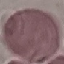
Summary:
  - Result: negative for malaria parasites
  - Preparation: thin blood film
  - Image type: automatically extracted cell patch, resized to 64 × 64 pixels
  - Capture: smartphone camera at the microscope eyepiece
  - Stain: Giemsa